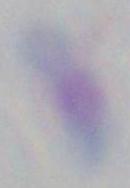 Captured at 1000x magnification. Photomicrograph. Toxoplasma gondii is seen.